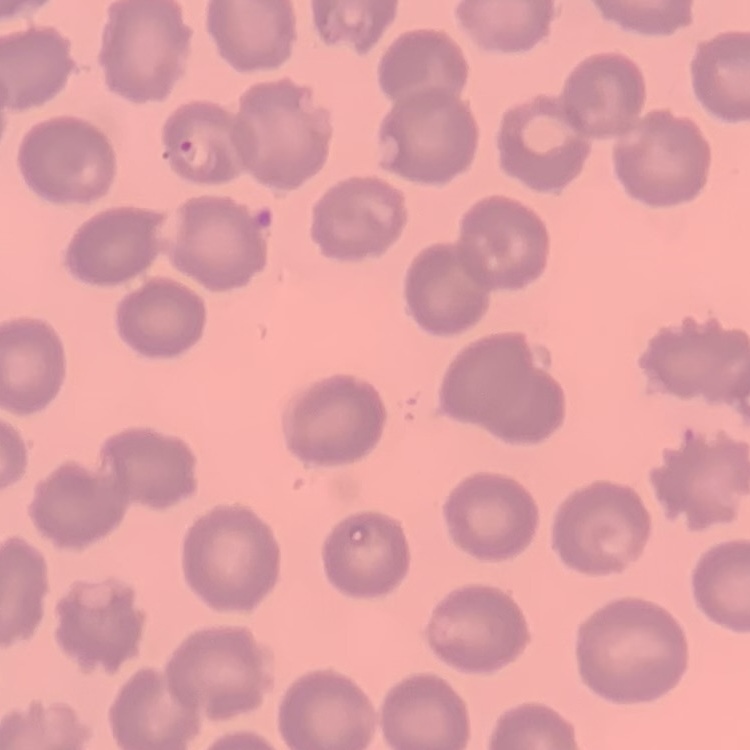
Summary:
  - Red blood cell morphology: no rouleaux formation
  - Image type: one tile cut from a larger photomicrograph
  - Preparation: thin blood film
  - Stain: Field's or Giemsa